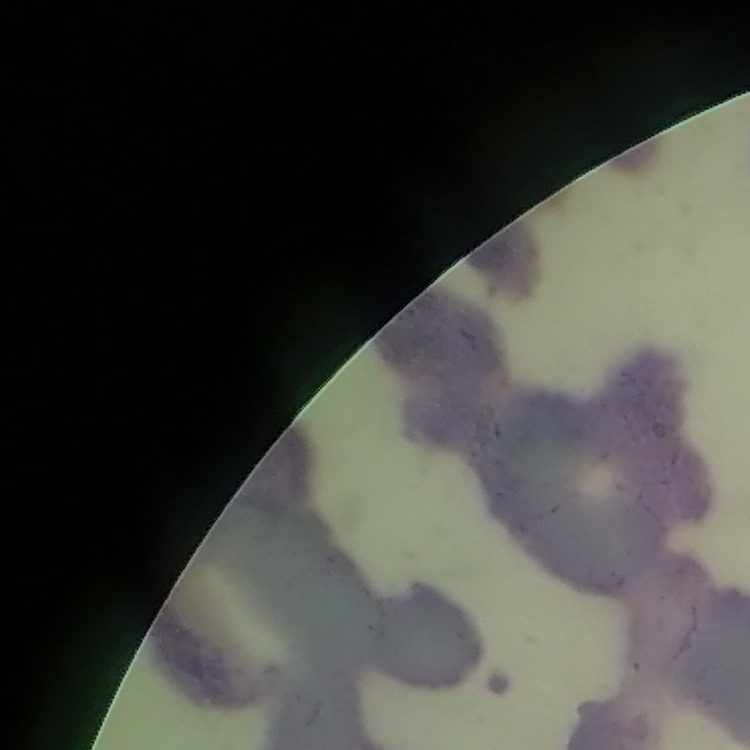
red_blood_cell_morphology: rouleaux formation
preparation: thin blood film
image_type: one tile cut from a larger photomicrograph
stain: Field's or Giemsa